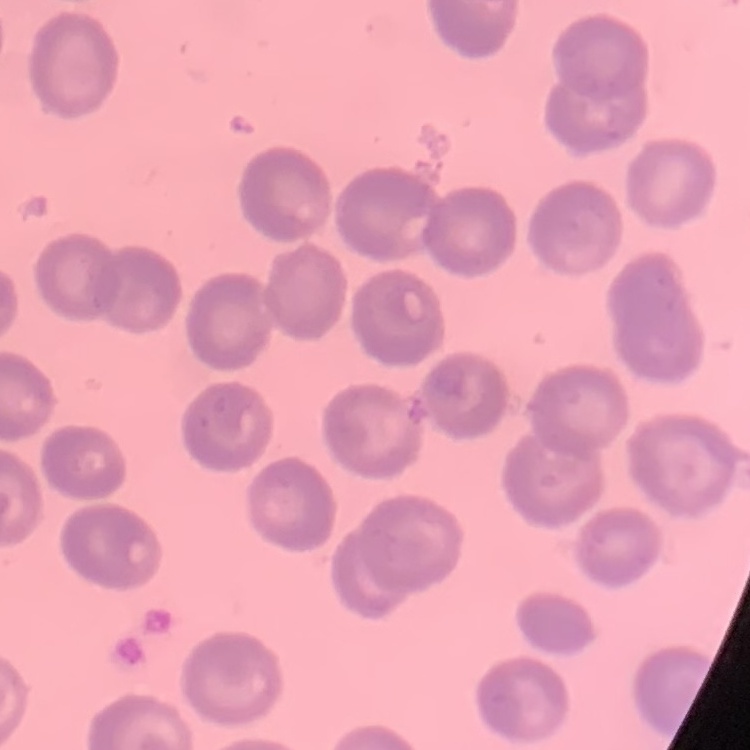

{
  "erythrocyte_morphology": "no rouleaux formation",
  "image_type": "one tile cut from a larger photomicrograph",
  "stain": "Field's or Giemsa",
  "preparation": "thin blood film"
}